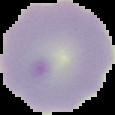

From a thin blood smear. Cell region segmented out of the field of view; the surrounding area is masked to black. Malaria status: uninfected. Image is 115×115 pixels.